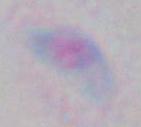
Summary:
  - Identification: Toxoplasma gondii
  - Magnification: 1000x
  - Modality: micrograph